Give the preparation type.
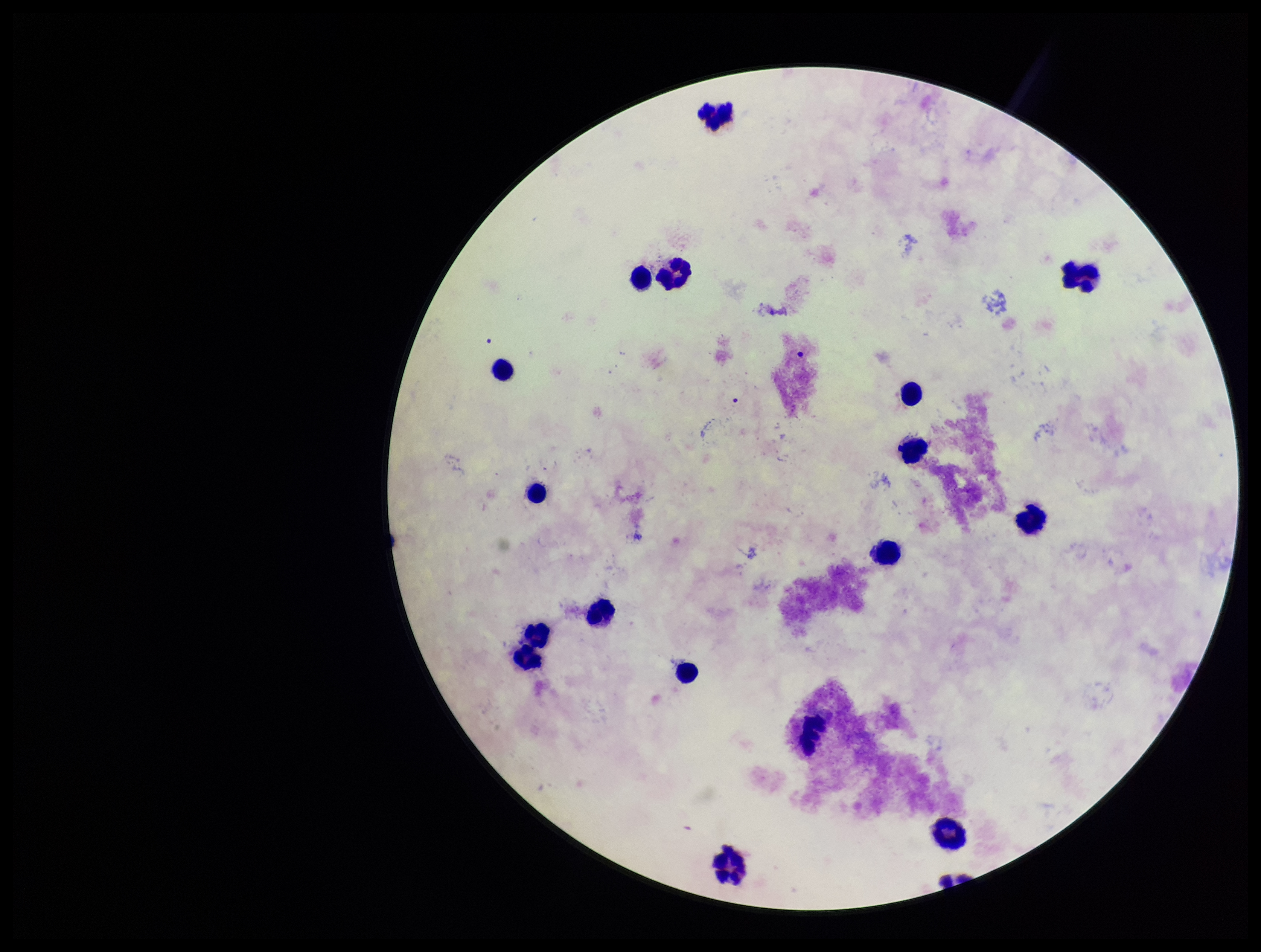

A thick smear.

{
  "stain": "Giemsa",
  "plasmodium_parasites": "none identified",
  "image_size": "1261×952 pixels",
  "patient_malaria_status": "negative",
  "leukocyte_count": 18,
  "field_of_view": "single",
  "capture": "smartphone photograph through the microscope eyepiece",
  "parasite_count": 0
}